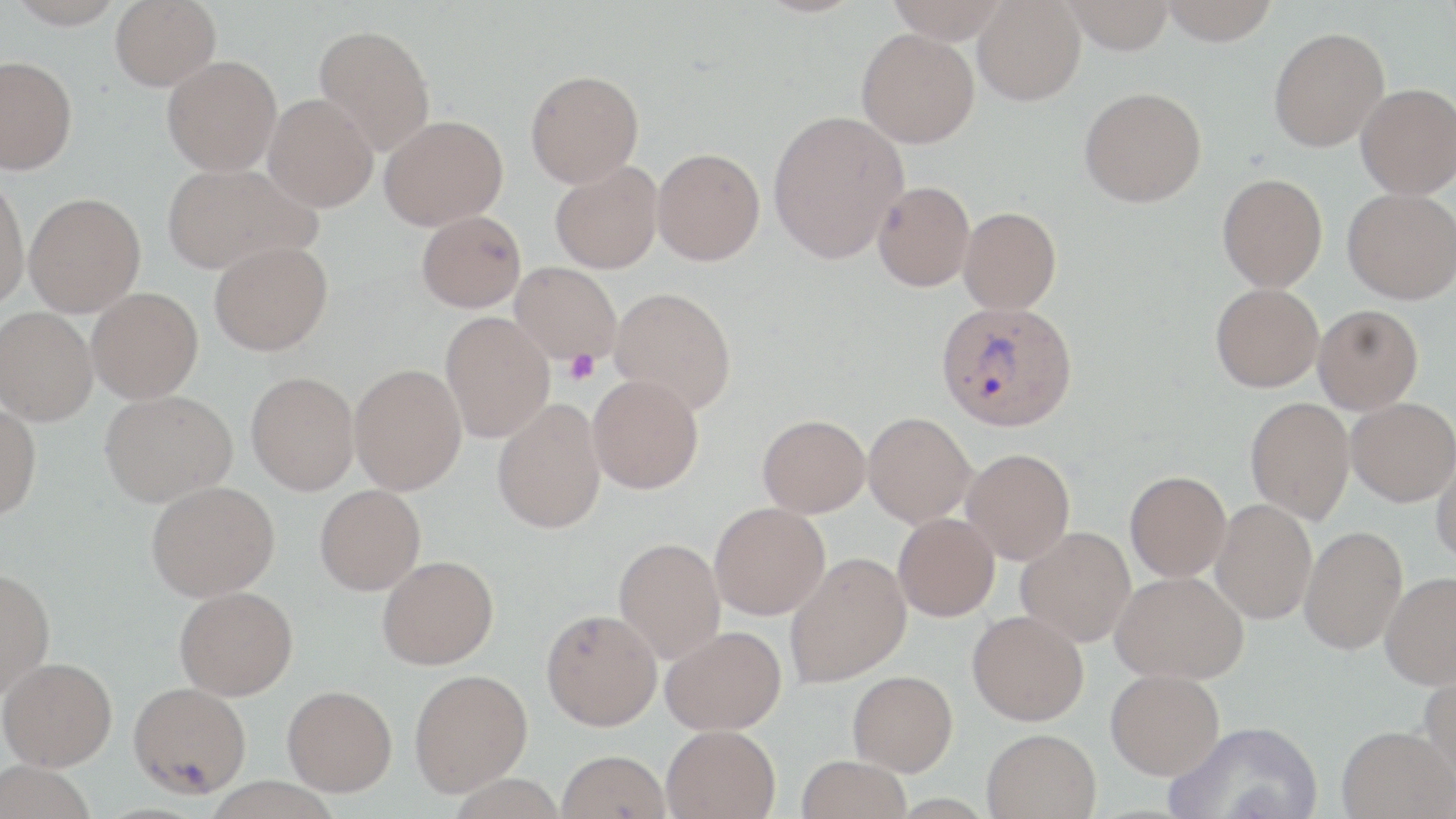

slide-level diagnosis = Plasmodium vivax
stain = May-Grünwald-Giemsa
platelet locations = approximate bounding boxes as [x1, y1, x2, y2] in pixels: [563, 349, 601, 384]
magnification = 1000x
preparation = thin blood smear
Plasmodium vivax-infected red blood cell locations = approximate bounding boxes as [x1, y1, x2, y2] in pixels: [936, 299, 1078, 431]
field of view = one of a larger specimen
uninfected red blood cell locations = approximate bounding boxes as [x1, y1, x2, y2] in pixels: [8, 0, 126, 29], [110, 0, 220, 90], [886, 0, 1010, 43], [1062, 0, 1176, 54], [1158, 0, 1280, 45], [973, 1, 1085, 105], [313, 23, 436, 155], [1268, 27, 1389, 152], [856, 28, 980, 148], [0, 55, 77, 174], [162, 55, 282, 175], [525, 69, 644, 187], [1356, 83, 1456, 199], [1079, 86, 1206, 207], [263, 94, 378, 212], [768, 109, 908, 263], [379, 114, 508, 230], [652, 147, 765, 265], [550, 160, 663, 274], [161, 162, 319, 275], [0, 173, 29, 311], [1217, 173, 1328, 292], [872, 180, 974, 291], [1342, 188, 1456, 304], [23, 192, 145, 317], [958, 207, 1061, 314], [416, 210, 526, 313], [209, 240, 332, 355], [510, 262, 622, 365], [1211, 283, 1323, 392], [610, 286, 737, 415], [87, 287, 203, 403], [1313, 304, 1423, 414], [0, 306, 98, 425], [440, 312, 555, 441], [349, 363, 467, 495], [246, 371, 359, 495], [587, 374, 704, 494], [99, 389, 237, 506], [1245, 396, 1354, 524], [1346, 397, 1456, 506], [493, 398, 606, 534], [0, 402, 42, 520], [863, 412, 976, 527], [758, 414, 870, 517], [1431, 447, 1456, 567], [961, 448, 1075, 565], [1125, 470, 1231, 581], [146, 480, 279, 601], [315, 484, 426, 595], [1211, 499, 1317, 624], [709, 502, 830, 620], [893, 513, 1000, 621], [1300, 525, 1407, 655], [1016, 527, 1135, 647], [613, 537, 725, 664], [784, 552, 911, 688], [377, 555, 499, 670], [0, 567, 55, 698], [1111, 570, 1248, 684], [1380, 570, 1456, 690], [174, 586, 298, 700], [542, 609, 662, 730], [967, 610, 1089, 726], [660, 625, 787, 735], [1, 657, 117, 770], [1417, 666, 1456, 793], [1106, 668, 1225, 779], [409, 669, 533, 797], [848, 670, 958, 776], [128, 681, 251, 798], [282, 685, 397, 795], [1167, 719, 1324, 819], [662, 724, 781, 819], [1337, 725, 1455, 819], [982, 728, 1101, 818], [557, 750, 671, 819], [797, 755, 911, 818], [0, 761, 97, 819]
image size = 1456×819 pixels
modality = light microscopy